Report the malaria status of this cell.
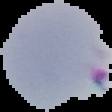
Parasitized.

From a thin blood film. Segmented cell region on a black background. Image is 112×112 pixels.